Outline each blood parasite and name the species.
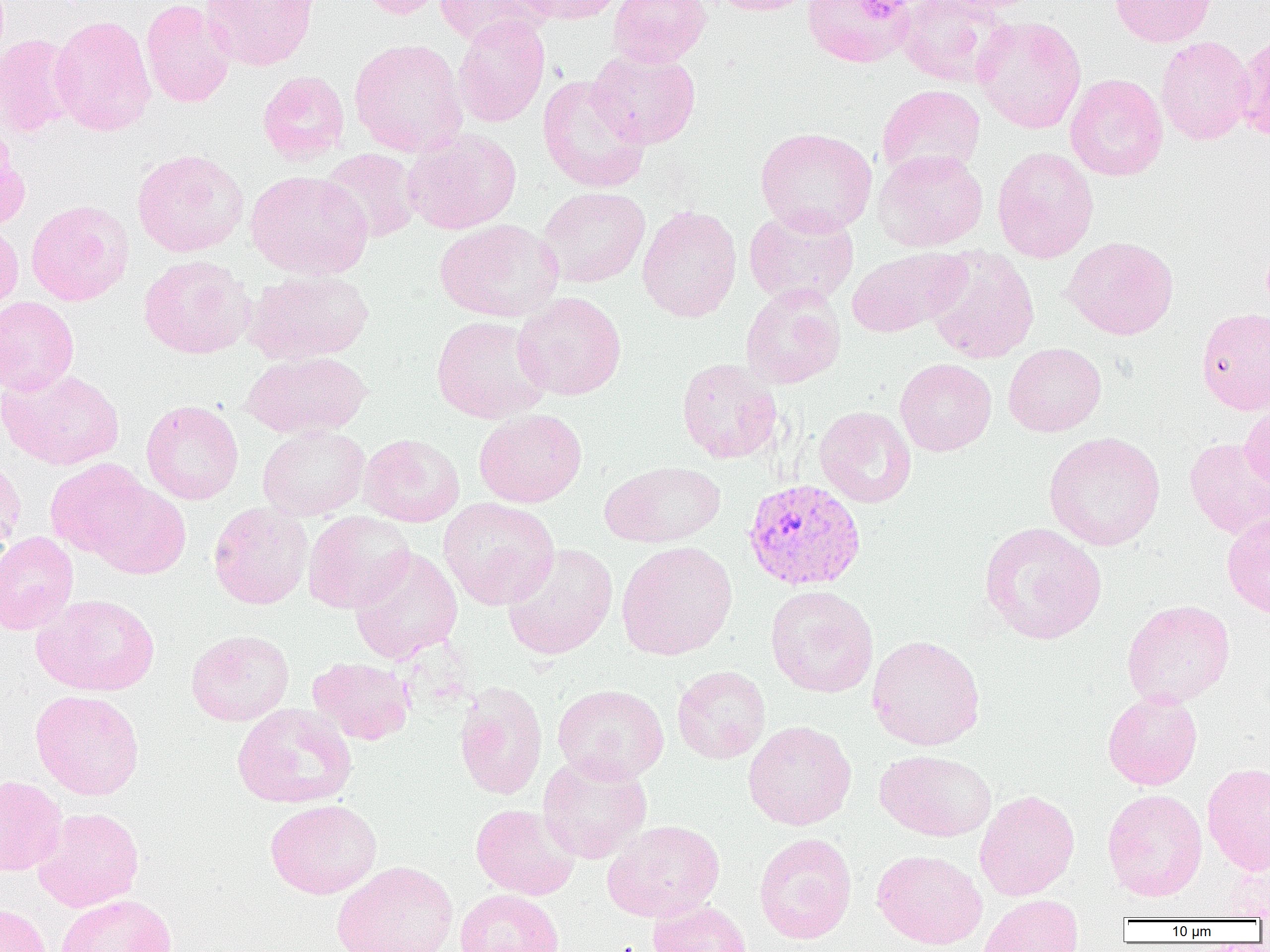

Approximate bounding boxes as [x1, y1, x2, y2] in pixels.
Plasmodium vivax-infected red blood cells: [742, 478, 867, 593].
No Plasmodium falciparum, Plasmodium ovale, Plasmodium malariae, Babesia divergens, or Trypanosoma brucei observed.

Uninfected red blood cell locations: [140, 0, 235, 108], [199, 0, 318, 71], [357, 0, 450, 19], [434, 0, 552, 48], [511, 0, 627, 24], [608, 0, 712, 68], [708, 0, 816, 16], [802, 0, 918, 68], [895, 0, 1009, 86], [931, 0, 1044, 14], [1109, 0, 1216, 47], [49, 14, 156, 136], [452, 15, 550, 128], [972, 15, 1087, 134], [0, 34, 78, 138], [1155, 36, 1254, 145], [349, 38, 468, 158], [586, 49, 701, 149], [257, 70, 350, 166], [1065, 74, 1168, 181], [537, 75, 650, 194], [877, 84, 986, 180], [755, 127, 877, 236], [0, 129, 30, 231], [403, 129, 522, 234], [992, 146, 1098, 263], [319, 148, 421, 243], [132, 149, 248, 257], [873, 149, 988, 252], [245, 170, 372, 279], [537, 187, 650, 288], [25, 200, 134, 306], [637, 204, 742, 323], [743, 207, 859, 307], [434, 219, 564, 323], [0, 222, 23, 316], [1062, 236, 1179, 340], [847, 247, 968, 338], [924, 248, 1040, 364], [138, 254, 254, 359], [244, 269, 375, 365], [740, 285, 845, 389], [513, 291, 627, 401], [0, 296, 79, 396], [1196, 307, 1270, 414], [430, 315, 551, 424], [1003, 343, 1106, 437], [241, 350, 371, 439], [676, 358, 781, 464], [895, 358, 997, 456], [1, 369, 125, 470], [141, 399, 244, 505], [1240, 401, 1270, 494], [814, 406, 916, 508], [474, 409, 587, 508], [258, 425, 370, 521], [1043, 432, 1165, 551], [358, 433, 465, 527], [1184, 437, 1270, 540], [0, 456, 26, 556], [45, 459, 152, 562], [601, 460, 726, 548], [83, 478, 191, 580], [438, 497, 559, 610], [208, 502, 313, 609], [303, 510, 415, 614], [1221, 511, 1270, 619], [979, 522, 1107, 645], [0, 531, 79, 635], [616, 541, 738, 661], [502, 543, 618, 660], [349, 547, 463, 665], [765, 586, 879, 698], [33, 593, 160, 696], [1122, 599, 1235, 708], [185, 629, 294, 726], [866, 634, 985, 751], [307, 657, 416, 745], [672, 665, 771, 764], [454, 681, 548, 800], [552, 684, 669, 784], [30, 689, 145, 800], [1103, 691, 1203, 790], [231, 702, 358, 809], [743, 720, 857, 830], [875, 750, 996, 841], [537, 753, 652, 863], [1202, 762, 1270, 876], [0, 775, 67, 875], [974, 789, 1079, 901], [1102, 789, 1207, 901], [264, 798, 382, 899], [470, 803, 580, 900], [33, 807, 144, 911], [602, 819, 725, 923], [753, 832, 857, 944], [872, 849, 988, 950], [1216, 854, 1270, 919], [331, 860, 459, 952], [455, 888, 564, 952], [55, 893, 177, 952], [978, 894, 1083, 952], [647, 899, 754, 952], [0, 902, 51, 952]. Platelet locations: [861, 4, 908, 26]. Slide-level diagnosis: Plasmodium vivax. One field of a larger specimen. 1000x magnification. Optical microscopy. Thin blood smear. Image is 1270×952 pixels.